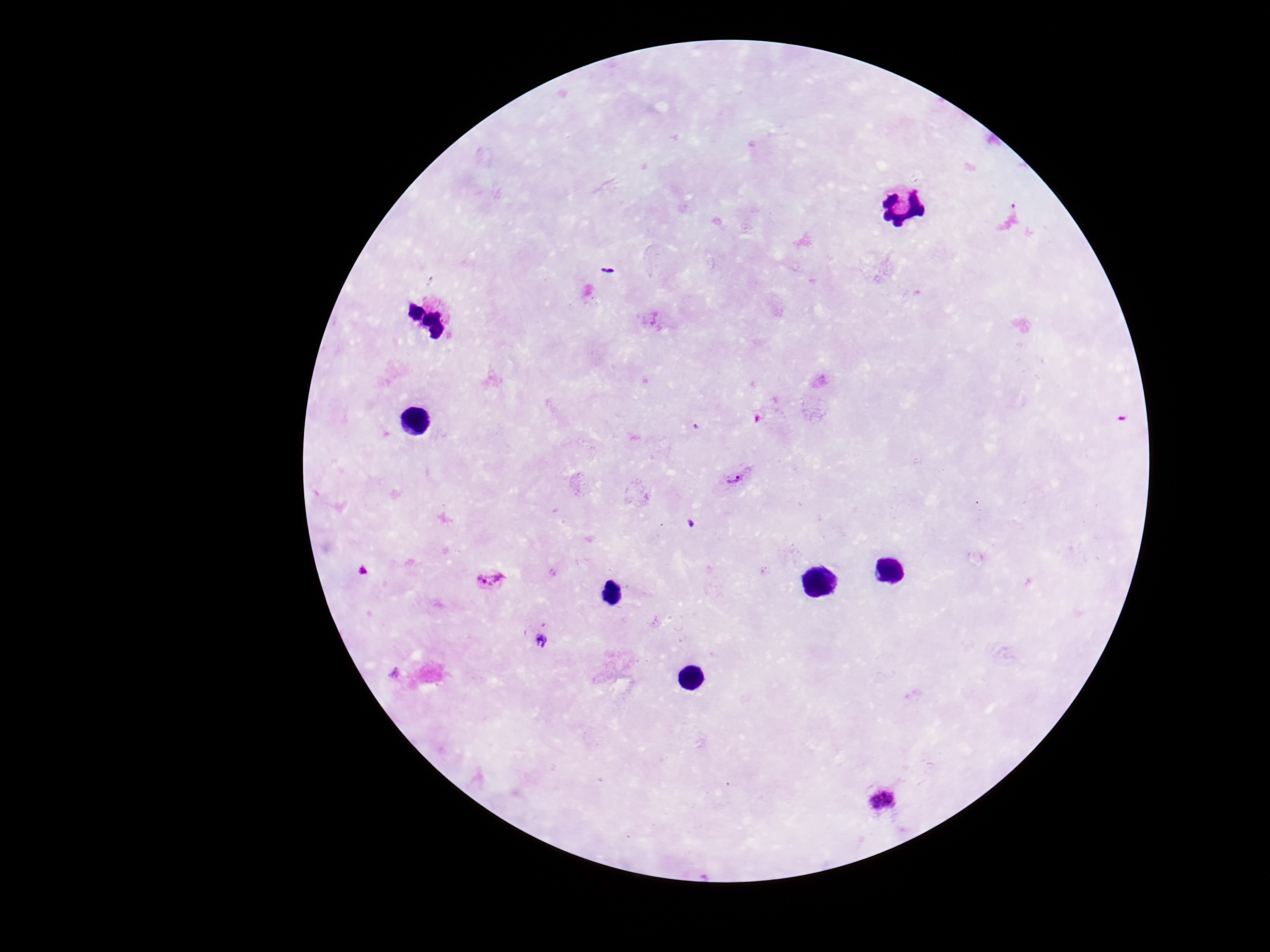
Approximate centers as (x, y) in pixels. Plasmodium parasite locations: (736, 480), (491, 581), (885, 801). Giemsa stain. Patient malaria status: infected. 100x magnification. Smartphone photograph taken through the microscope eyepiece. Thick peripheral-blood smear. Single field of view. Image is 1270×952 pixels.